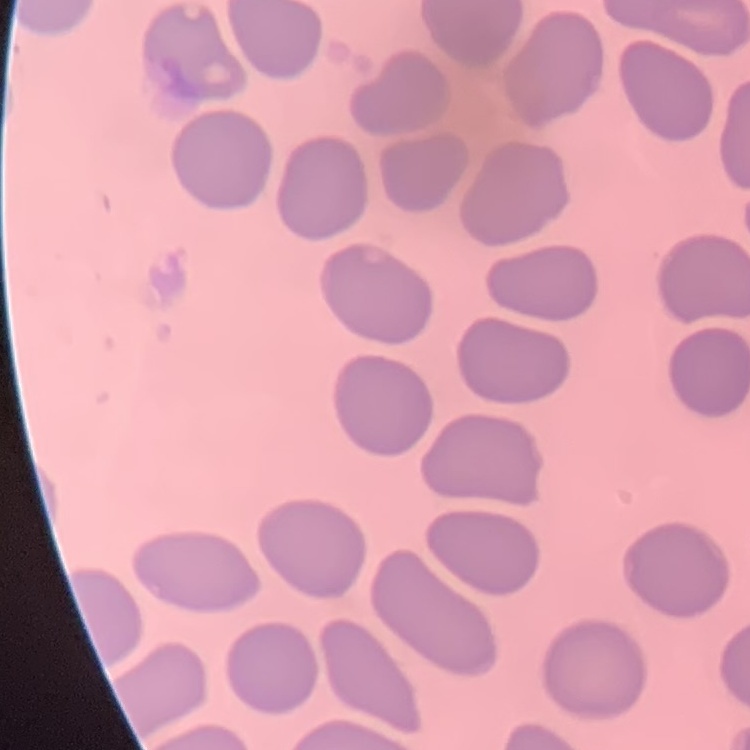
Summary:
  - Erythrocyte morphology: no rouleaux formation
  - Stain: Field's or Giemsa
  - Preparation: thin blood smear
  - Image type: one tile cut from a larger photomicrograph